Describe the morphology of the erythrocytes.
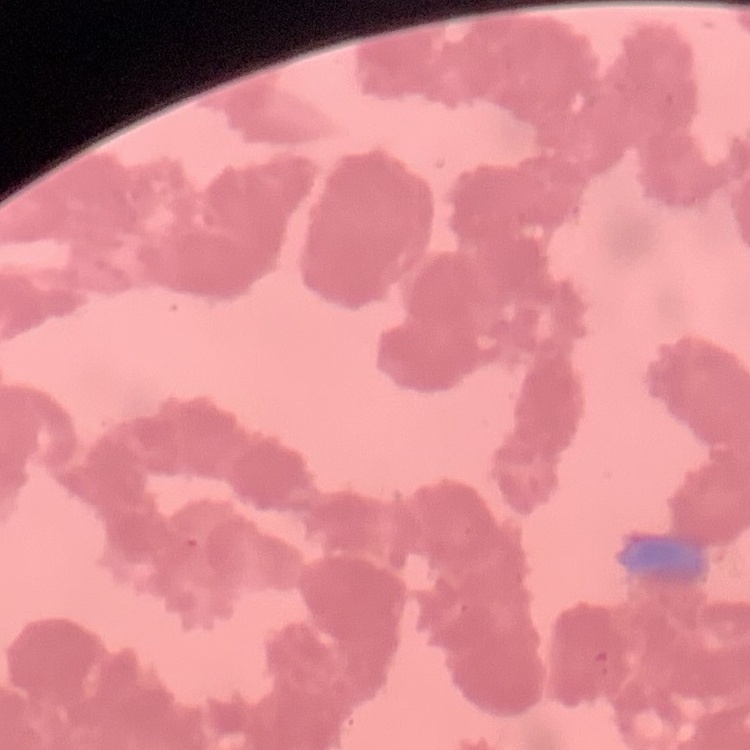
Rouleaux formation.

Summary:
  - Stain: Field's or Giemsa
  - Preparation: thin blood smear
  - Image type: square crop of a larger photomicrograph